Describe the morphology of the erythrocytes.
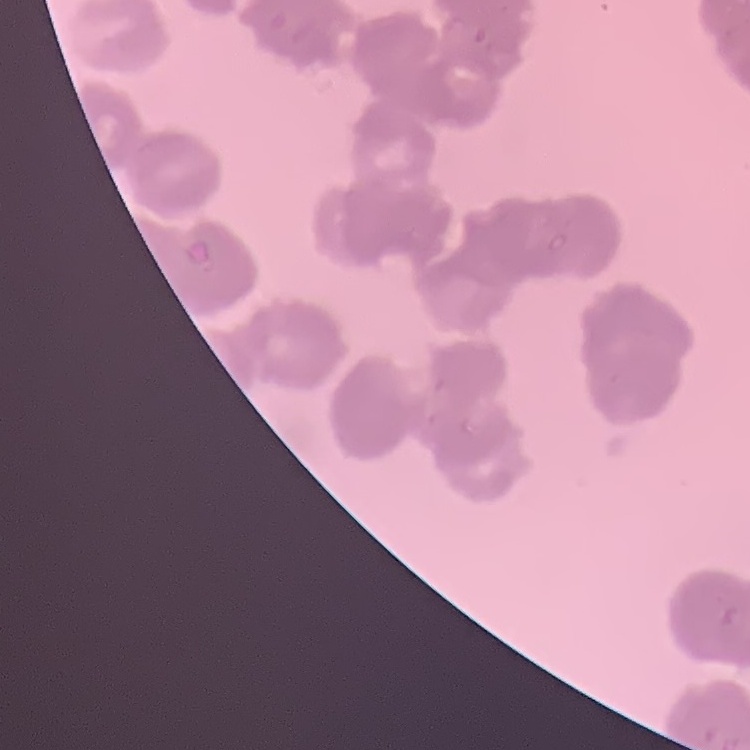
They show rouleaux formation.

{
  "preparation": "thin blood film",
  "image_type": "square crop of a larger photomicrograph",
  "stain": "Field's or Giemsa"
}